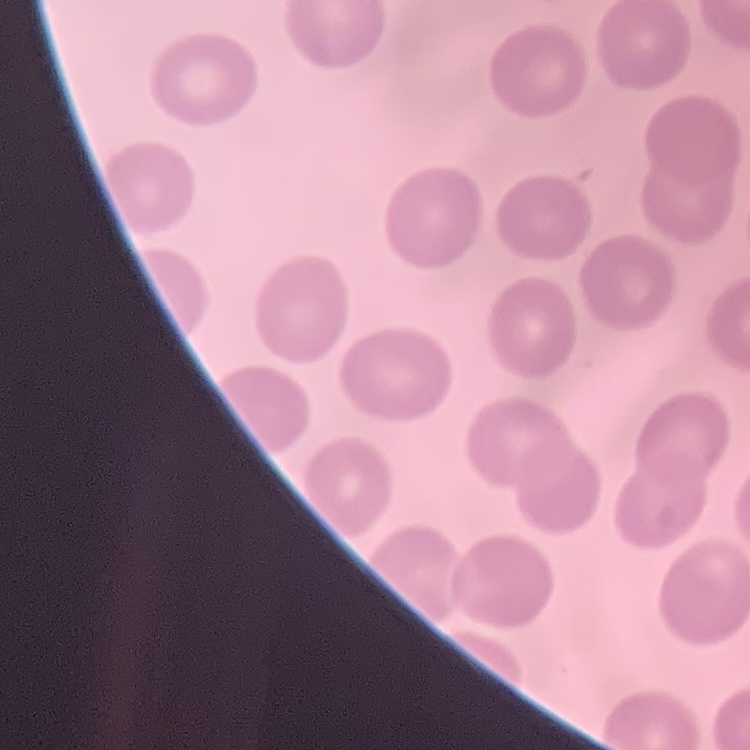

red blood cell morphology = no rouleaux formation
stain = Field's or Giemsa
preparation = thin peripheral smear
image type = one tile cut from a larger photomicrograph